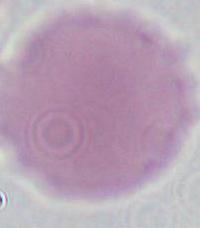

identification = red blood cell
modality = micrograph
magnification = 1000x